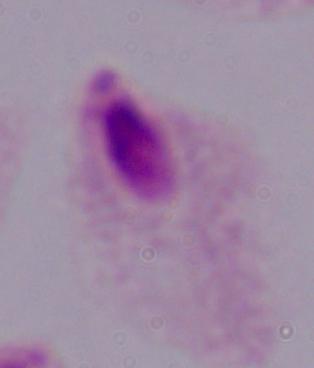

identification = trichomonad
modality = micrograph
magnification = 1000x